Name the cell type shown.
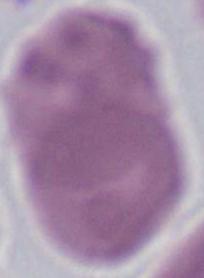

An erythrocyte.

Summary:
  - Magnification: 1000x
  - Modality: micrograph